Point out each Plasmodium parasite.
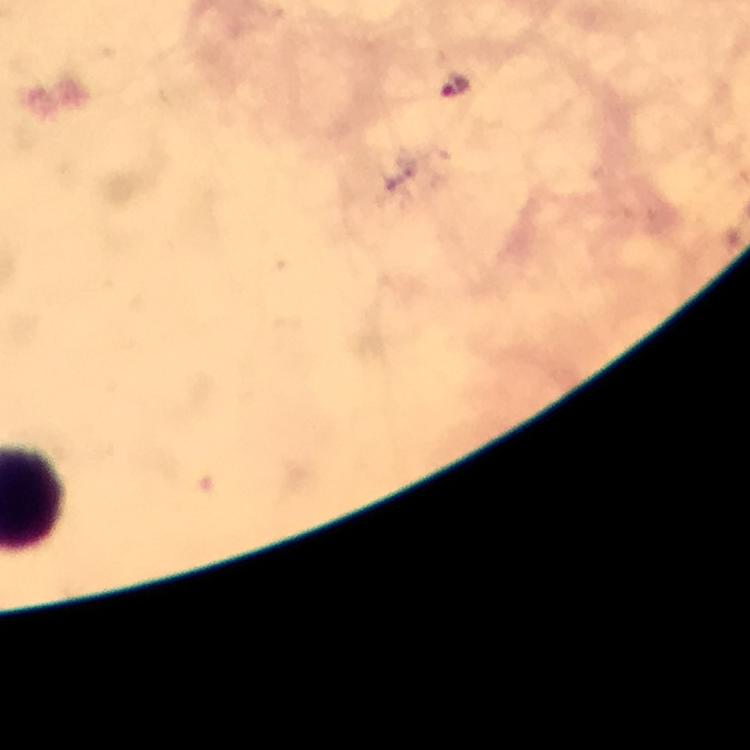
Approximate object centers, in pixels from the top-left corner.
Plasmodium parasites: (x=456, y=82).

{
  "context": "from a diagnostic examination for malaria",
  "magnification": "100x",
  "preparation": "thick smear",
  "immersion_oil": "applied",
  "stain": "Giemsa",
  "cropped_from": "one field of view",
  "image_size": "750×750 pixels",
  "capture": "smartphone camera through the microscope"
}